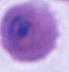 Photomicrograph. A Plasmodium parasite is shown. 400x or 1000x magnification.